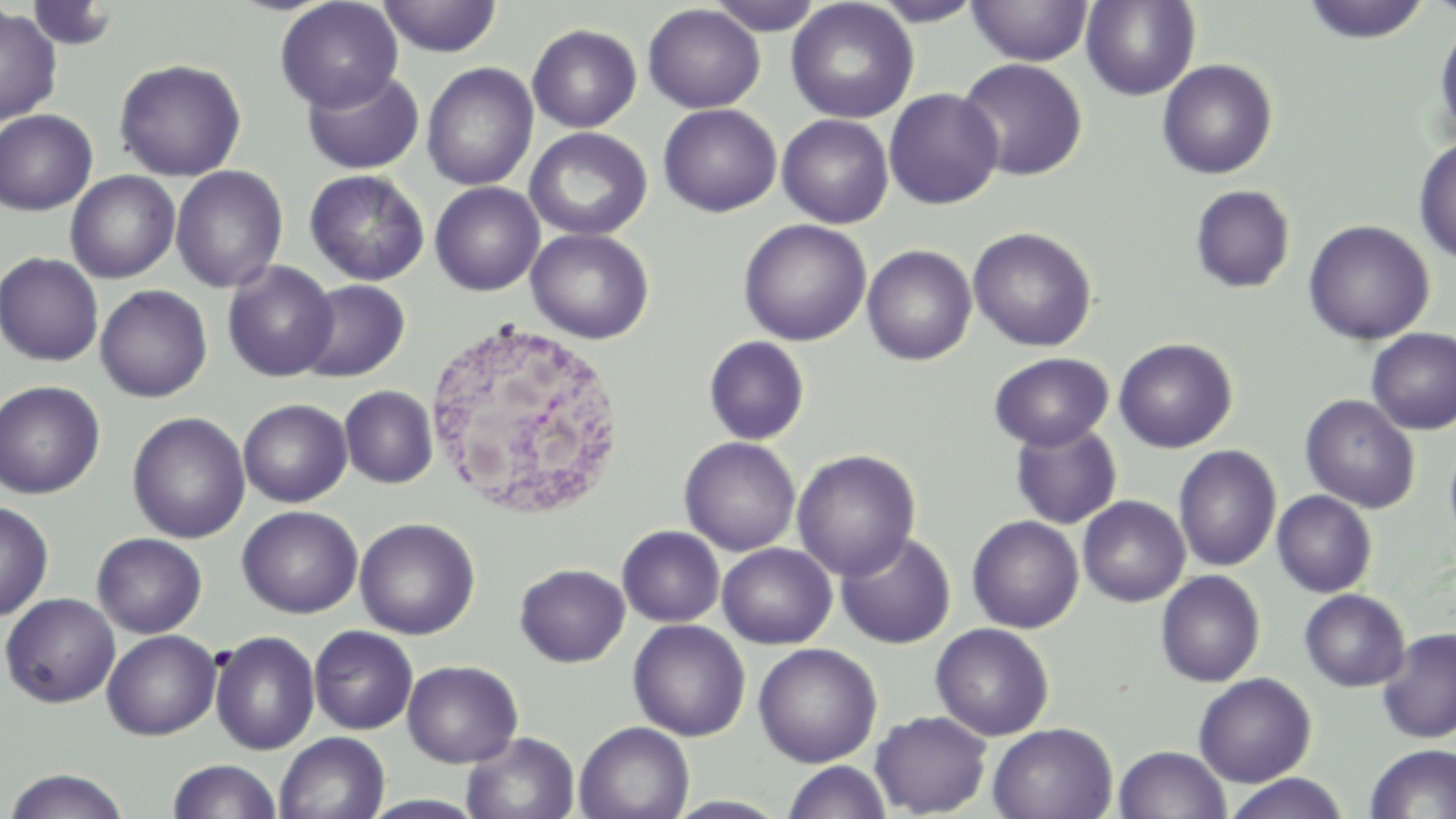 Approximate bounding boxes as (x1,y1)-(x2,y2) corner pairs in pixels. White blood cell locations: (420,317)-(628,522). Uninfected red blood cell locations: (275,0)-(403,113), (377,0)-(503,58), (707,0)-(824,35), (869,0)-(986,26), (967,0)-(1093,66), (1081,0)-(1199,100), (1301,0)-(1431,44), (786,1)-(919,123), (26,2)-(119,51), (643,4)-(765,113), (0,6)-(62,125), (1434,18)-(1456,144), (527,24)-(642,133), (114,59)-(247,181), (957,59)-(1088,181), (1157,59)-(1277,179), (422,63)-(539,191), (301,67)-(424,175), (883,88)-(1003,209), (658,104)-(782,217), (0,109)-(98,215), (777,114)-(894,228), (525,127)-(652,241), (1413,137)-(1456,266), (170,165)-(288,293), (305,169)-(429,285), (65,171)-(181,284), (429,182)-(544,296), (1190,185)-(1295,294), (737,219)-(871,346), (1303,219)-(1434,345), (968,226)-(1097,352), (526,228)-(655,344), (862,244)-(976,365), (0,252)-(104,367), (222,261)-(338,382), (296,279)-(410,382), (95,285)-(212,402), (1366,328)-(1456,435), (703,336)-(810,445), (1114,337)-(1238,453), (988,352)-(1114,451), (0,380)-(105,499), (340,385)-(438,488), (1300,395)-(1420,513), (238,399)-(352,507), (127,412)-(250,544), (1009,421)-(1122,529), (1444,433)-(1456,550), (680,437)-(801,556), (1173,445)-(1281,572), (792,449)-(921,580), (1272,490)-(1377,597), (1078,496)-(1190,607), (0,500)-(54,622), (237,506)-(362,618), (967,515)-(1084,633), (354,517)-(480,639), (617,526)-(724,627), (835,532)-(956,649), (92,533)-(208,638), (717,543)-(836,649), (515,563)-(629,667), (1155,570)-(1265,687), (1299,588)-(1410,691), (0,592)-(121,708), (627,619)-(750,741), (931,623)-(1054,741), (309,626)-(418,734), (1377,628)-(1456,743), (102,630)-(221,740), (209,630)-(320,755), (753,643)-(882,767), (402,660)-(523,767), (1193,672)-(1316,787), (870,710)-(992,817), (574,721)-(694,819), (987,723)-(1118,819), (275,732)-(390,819), (461,732)-(580,818), (1363,743)-(1456,818), (1114,745)-(1230,819), (168,759)-(281,819), (782,761)-(892,819), (2,769)-(132,819), (1222,773)-(1350,819). Slide-level diagnosis: no evidence of blood parasites. Light microscopy. 1000x magnification. Thin blood film. Single field of view. May-Grünwald-Giemsa-stained preparation. Image is 1456×819 pixels.